Classify this cell by malaria status.
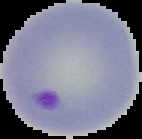
Parasitized.

Segmented cell region on a black background. Image is 142×139 pixels. From a thin blood film.